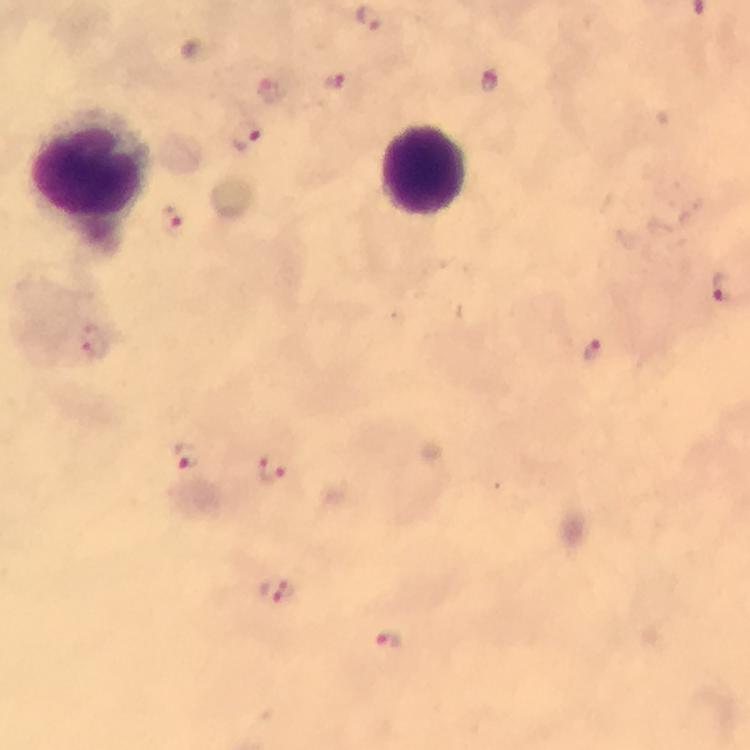

Approximate object centers, in pixels from the top-left corner.
Summary:
  - Plasmodium parasite locations: (x=333, y=81), (x=247, y=135), (x=171, y=222), (x=725, y=288), (x=593, y=350), (x=187, y=457), (x=270, y=469), (x=280, y=591), (x=390, y=640)
  - Leukocyte locations: (x=423, y=170), (x=89, y=172)
  - Context: from a diagnostic examination for malaria
  - Stain: Giemsa
  - Magnification: 100x
  - Immersion oil: applied
  - Image size: 750×750 pixels
  - Cropped from: one field of view
  - Preparation: thick smear
  - Capture: smartphone mounted on the microscope